Locate every blood parasite and identify its species.
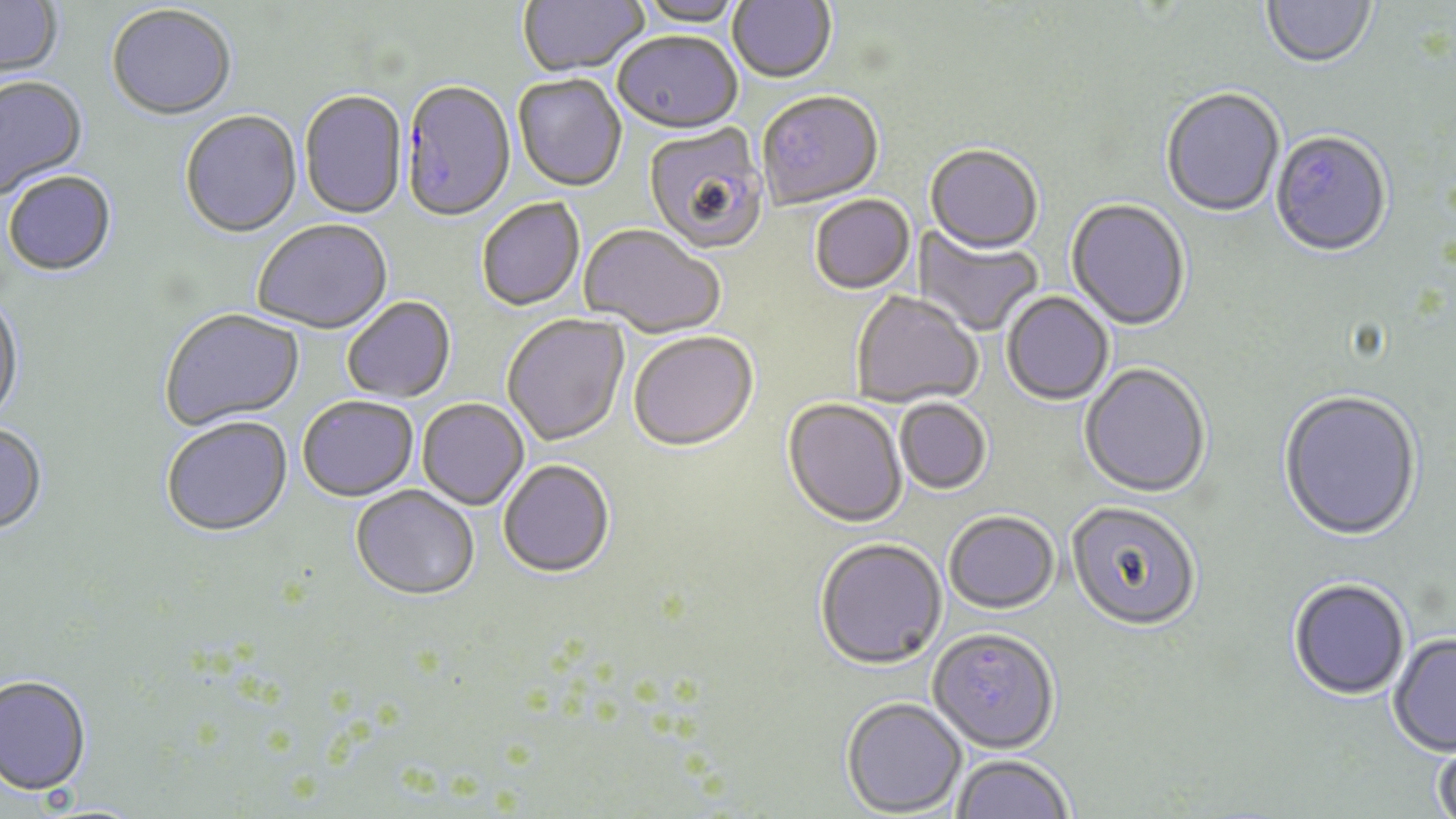
Approximate bounding boxes as (x1, y1, x2, y2) in pixels.
Plasmodium falciparum-infected red blood cells: (400, 82, 516, 225).
No Plasmodium ovale, Plasmodium malariae, Plasmodium vivax, Babesia divergens, or Trypanosoma brucei observed.

slide-level diagnosis = Plasmodium falciparum
image size = 1456×819 pixels
preparation = thin blood smear
uninfected red blood cell locations = approximate bounding boxes as (x1, y1, x2, y2) in pixels: (517, 0, 649, 79), (636, 0, 746, 29), (728, 0, 836, 85), (1262, 0, 1376, 72), (0, 1, 63, 80), (106, 7, 237, 123), (612, 34, 742, 136), (513, 75, 627, 194), (0, 78, 89, 199), (1161, 90, 1285, 219), (299, 92, 407, 221), (758, 92, 884, 211), (180, 112, 302, 240), (643, 124, 769, 256), (1270, 133, 1393, 260), (925, 147, 1043, 256), (3, 173, 117, 278), (810, 196, 916, 296), (477, 199, 585, 312), (1065, 200, 1191, 333), (252, 222, 394, 336), (911, 224, 1043, 337), (579, 226, 725, 340), (851, 292, 983, 409), (1001, 292, 1114, 406), (0, 295, 25, 428), (342, 298, 456, 404), (160, 310, 305, 432), (502, 315, 630, 448), (628, 334, 759, 455), (1079, 365, 1212, 500), (1278, 392, 1422, 544), (298, 398, 419, 503), (781, 399, 907, 530), (894, 399, 991, 496), (417, 400, 529, 511), (161, 419, 292, 540), (0, 425, 48, 537), (498, 462, 615, 580), (351, 487, 480, 602), (1066, 503, 1201, 634), (944, 514, 1060, 616), (813, 541, 947, 673), (1287, 580, 1411, 703), (928, 632, 1059, 755), (1388, 635, 1456, 757), (0, 677, 91, 797), (841, 698, 967, 817), (1432, 738, 1456, 819), (953, 756, 1074, 818)
stain = May-Grünwald-Giemsa
field of view = single
magnification = 1000x
modality = optical microscopy